Evaluate for malaria.
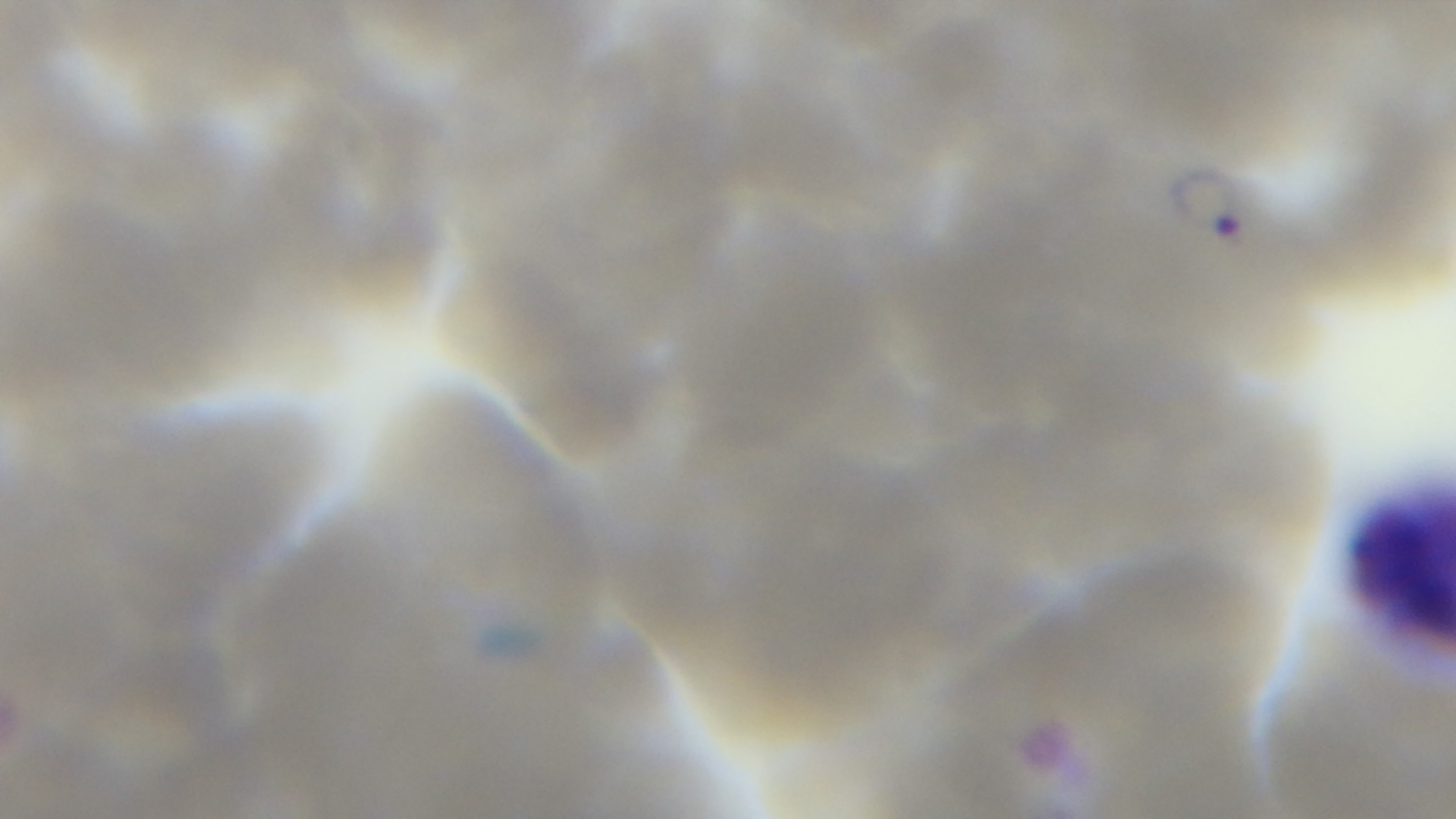
It is infected.

Summary:
  - Objective: 100x oil immersion
  - Capture: mounted 4K digital camera
  - Stain: Giemsa
  - Preparation: thin smear
  - Field of view: one from the slide
  - Modality: light microscopy